Outline each blood parasite and name the species.
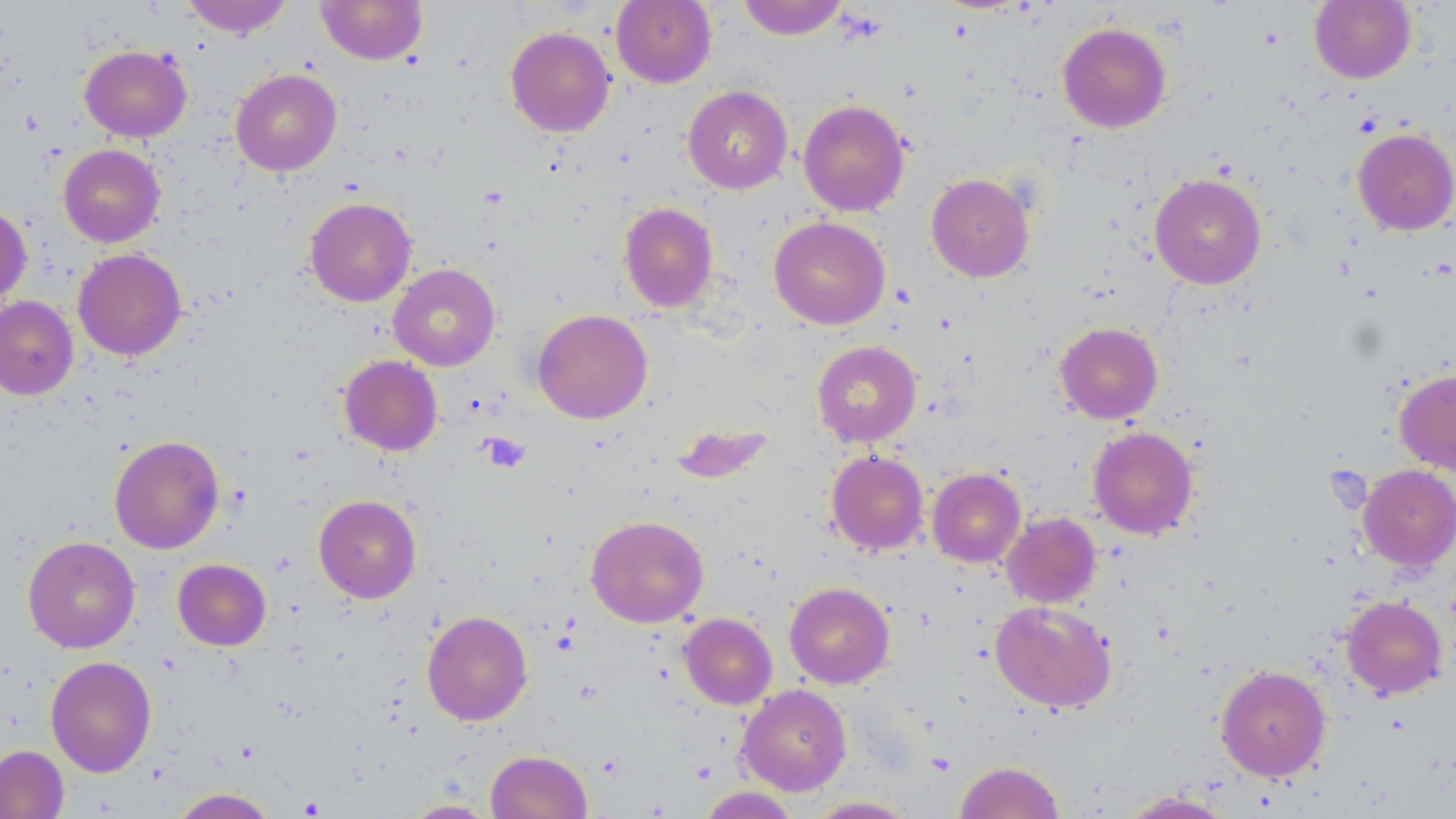

No blood parasites seen.

Approximate bounding boxes as (x1, y1, x2, y2) in pixels. Platelet locations: (482, 433, 530, 472). Uninfected red blood cell locations: (181, 0, 293, 38), (316, 0, 427, 65), (611, 0, 716, 88), (737, 0, 848, 40), (1309, 0, 1415, 84), (1057, 22, 1172, 133), (505, 26, 615, 137), (79, 44, 192, 142), (231, 69, 342, 176), (682, 86, 793, 194), (798, 99, 910, 216), (1352, 128, 1456, 236), (58, 144, 166, 247), (926, 173, 1035, 282), (1150, 173, 1266, 289), (304, 197, 417, 307), (0, 202, 32, 307), (618, 202, 718, 312), (769, 217, 890, 330), (72, 248, 187, 361), (388, 263, 500, 371), (0, 295, 78, 400), (533, 309, 653, 424), (1054, 321, 1163, 424), (811, 340, 921, 447), (339, 354, 442, 456), (1394, 369, 1456, 475), (670, 422, 774, 484), (1087, 425, 1198, 540), (109, 434, 225, 554), (826, 450, 929, 555), (1357, 464, 1456, 571), (927, 467, 1026, 568), (313, 494, 421, 603), (1001, 512, 1101, 608), (585, 515, 709, 627), (23, 535, 140, 653), (173, 558, 271, 650), (784, 582, 895, 688), (1340, 595, 1447, 699), (990, 600, 1117, 713), (422, 610, 533, 725), (679, 613, 777, 709), (45, 655, 157, 777), (1215, 663, 1331, 781), (737, 684, 852, 795), (0, 745, 69, 819), (486, 749, 592, 819), (954, 760, 1065, 819), (697, 787, 799, 818), (168, 788, 279, 818), (1118, 790, 1235, 818), (805, 796, 918, 818), (402, 799, 496, 818). Slide-level diagnosis: negative for blood parasites. Light microscopy. Thin blood film. Single field of view. Image is 1456×819 pixels. May-Grünwald-Giemsa stain. 1000x magnification.